Outline each blood parasite and name the species.
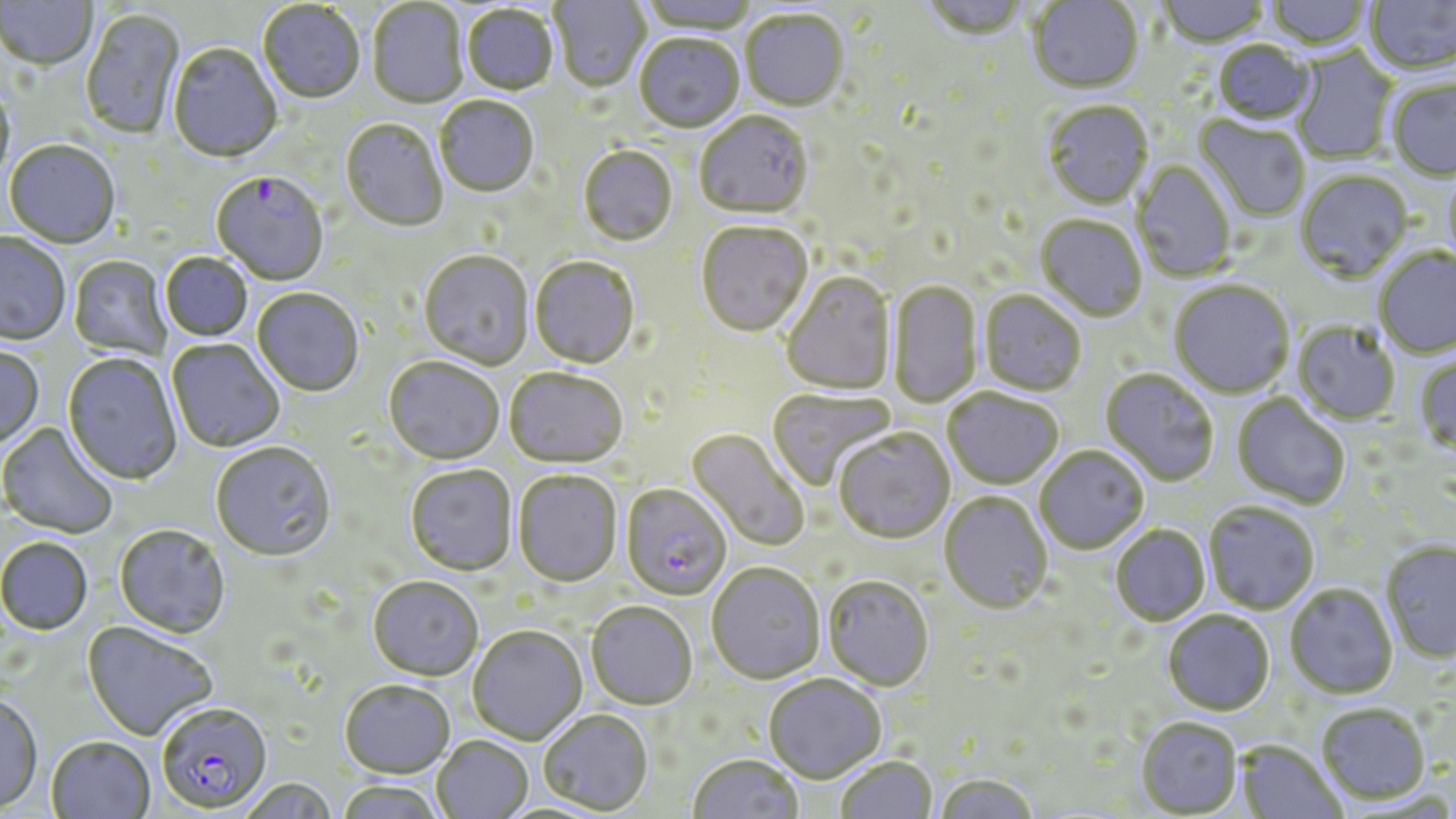

Approximate bounding boxes as (x1, y1, x2, y2) in pixels.
Plasmodium falciparum-infected red blood cells: (211, 173, 328, 287), (620, 485, 731, 602), (156, 705, 272, 815).
No Plasmodium ovale, Plasmodium malariae, Plasmodium vivax, Babesia divergens, or Trypanosoma brucei observed.

slide_level_diagnosis: Plasmodium falciparum
modality: optical microscopy
preparation: thin blood smear
uninfected_red_blood_cell_locations: 'approximate bounding boxes as (x1, y1, x2, y2) in pixels: (550, 0, 651, 94), (637, 0, 759, 35), (920, 0, 1030, 44), (1028, 0, 1143, 95), (1158, 0, 1268, 49), (1265, 0, 1372, 52), (1365, 0, 1456, 76), (1, 1, 98, 72), (258, 2, 365, 106), (368, 2, 467, 109), (462, 6, 558, 97), (81, 9, 186, 141), (741, 12, 848, 113), (635, 36, 743, 135), (1212, 42, 1317, 129), (168, 45, 282, 164), (1291, 46, 1398, 164), (1387, 78, 1456, 182), (0, 80, 16, 187), (435, 98, 538, 199), (1042, 102, 1154, 211), (695, 114, 813, 221), (1194, 116, 1309, 222), (340, 120, 447, 233), (4, 142, 120, 250), (578, 148, 678, 248), (1131, 160, 1235, 282), (1442, 171, 1456, 270), (1295, 172, 1413, 283), (1035, 216, 1147, 324), (696, 223, 813, 339), (0, 233, 70, 347), (1374, 249, 1456, 359), (419, 252, 534, 371), (160, 253, 253, 342), (68, 257, 171, 361), (529, 258, 640, 371), (781, 273, 897, 397), (887, 281, 983, 408), (1169, 282, 1294, 400), (252, 289, 363, 398), (979, 291, 1086, 398), (1292, 322, 1400, 426), (167, 340, 284, 453), (0, 346, 44, 450), (62, 354, 182, 486), (1415, 355, 1456, 456), (383, 359, 504, 467), (505, 370, 627, 471), (1100, 370, 1218, 487), (767, 388, 896, 491), (942, 390, 1063, 490), (1232, 394, 1350, 509), (0, 422, 118, 539), (685, 427, 810, 553), (834, 430, 955, 546), (211, 444, 337, 564), (1035, 447, 1149, 555), (405, 466, 516, 577), (512, 472, 623, 589), (939, 494, 1052, 616), (1204, 503, 1319, 615), (1111, 525, 1211, 627), (114, 526, 231, 640), (0, 538, 93, 636), (1380, 541, 1456, 663), (707, 564, 825, 686), (822, 578, 934, 693), (367, 579, 482, 683), (1285, 585, 1398, 700), (586, 604, 696, 712), (1163, 612, 1275, 717), (82, 622, 218, 742), (468, 627, 587, 746), (764, 676, 886, 785), (340, 681, 455, 781), (0, 693, 44, 815), (1316, 704, 1430, 806), (537, 711, 653, 816), (1136, 718, 1243, 817), (46, 737, 156, 819), (431, 737, 532, 819), (1236, 741, 1347, 818), (687, 756, 803, 819), (836, 757, 937, 818), (934, 776, 1039, 819), (237, 779, 338, 819), (335, 782, 446, 819)'
magnification: 1000x
field_of_view: one of a larger specimen
stain: May-Grünwald-Giemsa
image_size: 1456×819 pixels